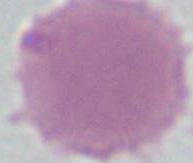

Photomicrograph. A red blood cell is seen. 1000x magnification.